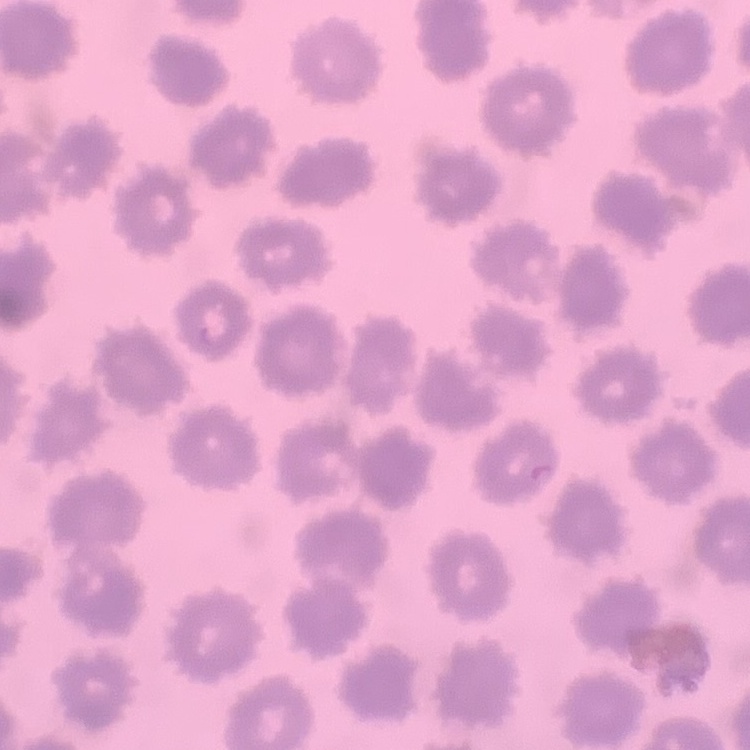

erythrocyte morphology = no rouleaux formation
image type = square crop of a larger photomicrograph
preparation = thin blood film
stain = Field's or Giemsa